Report the malaria status of this cell.
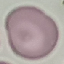

Uninfected.

Summary:
  - Preparation: thin blood smear
  - Stain: Giemsa
  - Capture: smartphone camera at the microscope eyepiece
  - Image type: cell patch, automatically extracted from a larger field of view and resized to 64 × 64 pixels